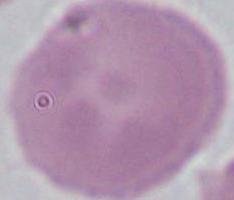
Summary:
  - Magnification: 1000x
  - Identification: red blood cell
  - Modality: photomicrograph